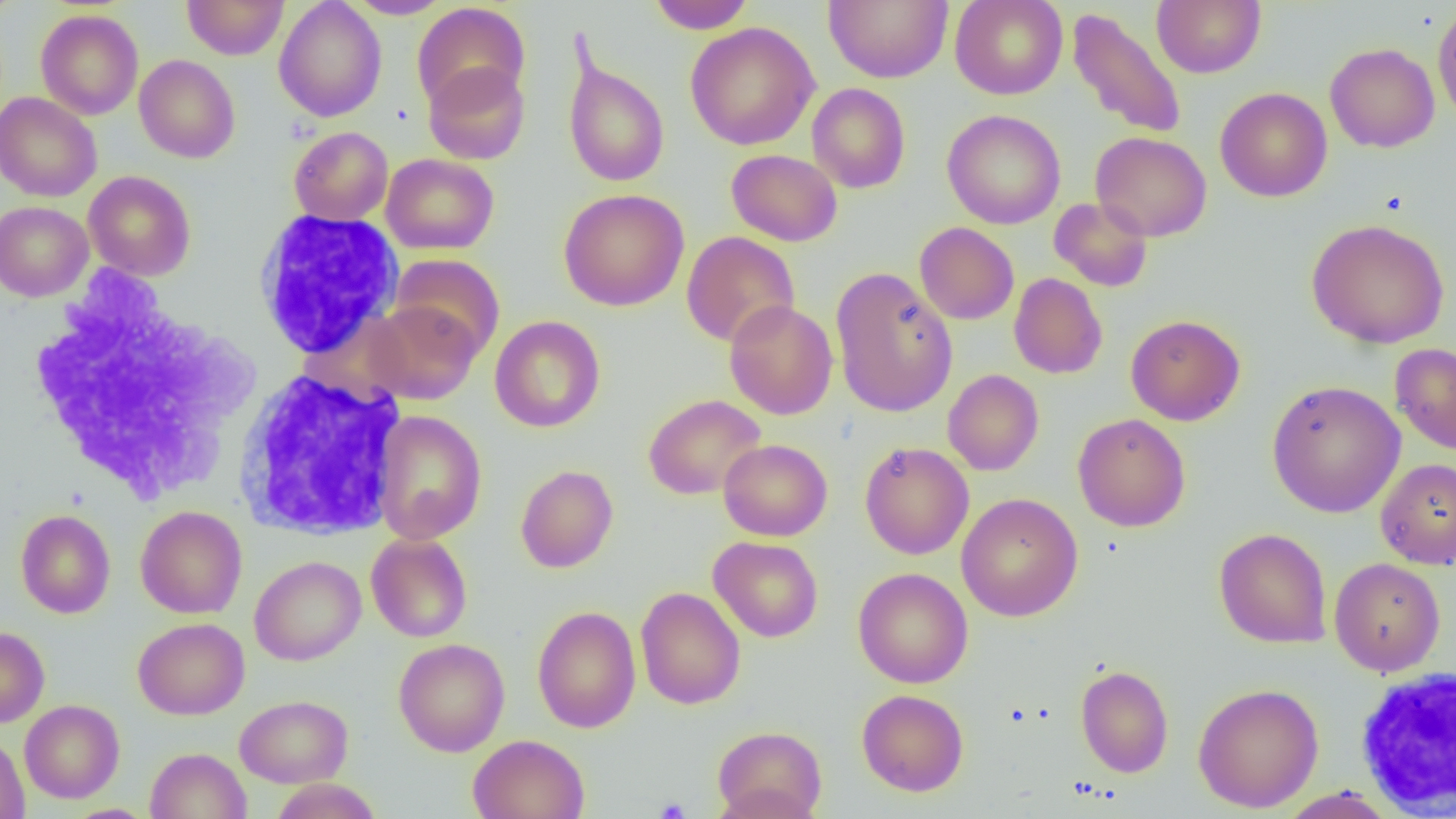
slide-level diagnosis = no evidence of blood parasites
platelet locations = approximate bounding boxes as named x1/y1/x2/y2 corners in pixels: (x1=655, y1=798, x2=691, y2=819)
image size = 1456×819 pixels
uninfected red blood cell locations = approximate bounding boxes as named x1/y1/x2/y2 corners in pixels: (x1=182, y1=0, x2=288, y2=59), (x1=274, y1=0, x2=387, y2=122), (x1=344, y1=0, x2=451, y2=19), (x1=646, y1=0, x2=756, y2=33), (x1=823, y1=0, x2=953, y2=84), (x1=950, y1=0, x2=1067, y2=100), (x1=1152, y1=0, x2=1265, y2=78), (x1=412, y1=3, x2=530, y2=111), (x1=950, y1=5, x2=1189, y2=111), (x1=1432, y1=5, x2=1456, y2=126), (x1=1067, y1=6, x2=1187, y2=140), (x1=36, y1=9, x2=144, y2=119), (x1=685, y1=22, x2=820, y2=150), (x1=1325, y1=43, x2=1440, y2=152), (x1=563, y1=49, x2=670, y2=188), (x1=134, y1=55, x2=240, y2=163), (x1=423, y1=61, x2=530, y2=165), (x1=807, y1=83, x2=910, y2=193), (x1=1215, y1=87, x2=1332, y2=202), (x1=0, y1=93, x2=101, y2=201), (x1=942, y1=109, x2=1066, y2=230), (x1=289, y1=126, x2=393, y2=225), (x1=1090, y1=131, x2=1212, y2=242), (x1=726, y1=149, x2=842, y2=246), (x1=381, y1=153, x2=499, y2=254), (x1=84, y1=170, x2=196, y2=280), (x1=558, y1=188, x2=689, y2=311), (x1=1049, y1=198, x2=1153, y2=292), (x1=0, y1=201, x2=93, y2=301), (x1=1306, y1=218, x2=1450, y2=349), (x1=915, y1=222, x2=1019, y2=325), (x1=681, y1=231, x2=800, y2=348), (x1=389, y1=253, x2=506, y2=359), (x1=830, y1=267, x2=958, y2=417), (x1=1009, y1=273, x2=1108, y2=379), (x1=365, y1=300, x2=482, y2=405), (x1=724, y1=300, x2=838, y2=420), (x1=1125, y1=314, x2=1245, y2=425), (x1=489, y1=315, x2=605, y2=433), (x1=1390, y1=343, x2=1456, y2=455), (x1=943, y1=369, x2=1044, y2=475), (x1=1266, y1=380, x2=1406, y2=518), (x1=643, y1=394, x2=766, y2=500), (x1=372, y1=410, x2=487, y2=544), (x1=1072, y1=413, x2=1191, y2=532), (x1=718, y1=439, x2=833, y2=541), (x1=859, y1=442, x2=974, y2=559), (x1=1375, y1=457, x2=1456, y2=570), (x1=515, y1=465, x2=618, y2=573), (x1=956, y1=493, x2=1083, y2=622), (x1=135, y1=505, x2=247, y2=619), (x1=15, y1=509, x2=116, y2=618), (x1=1214, y1=527, x2=1332, y2=649), (x1=366, y1=533, x2=473, y2=643), (x1=709, y1=536, x2=823, y2=642), (x1=250, y1=555, x2=366, y2=666), (x1=1328, y1=558, x2=1445, y2=676), (x1=852, y1=567, x2=973, y2=688), (x1=635, y1=587, x2=746, y2=709), (x1=532, y1=605, x2=641, y2=733), (x1=133, y1=617, x2=249, y2=720), (x1=0, y1=626, x2=49, y2=727), (x1=394, y1=638, x2=510, y2=757), (x1=1075, y1=664, x2=1174, y2=777), (x1=1193, y1=683, x2=1323, y2=812), (x1=856, y1=689, x2=969, y2=796), (x1=235, y1=694, x2=353, y2=787), (x1=20, y1=700, x2=124, y2=803), (x1=712, y1=725, x2=827, y2=819), (x1=0, y1=732, x2=30, y2=819), (x1=468, y1=734, x2=589, y2=819), (x1=145, y1=748, x2=251, y2=819), (x1=269, y1=778, x2=382, y2=818), (x1=1277, y1=788, x2=1397, y2=818), (x1=61, y1=804, x2=159, y2=819)
magnification = 1000x
modality = light microscopy
field of view = one of a larger specimen
preparation = thin blood film
white blood cell locations = approximate bounding boxes as named x1/y1/x2/y2 corners in pixels: (x1=252, y1=210, x2=402, y2=359), (x1=24, y1=269, x2=260, y2=505), (x1=233, y1=368, x2=407, y2=541), (x1=1352, y1=665, x2=1456, y2=815)